Identify the parasite.
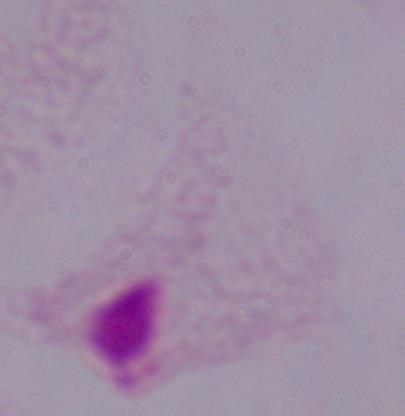

A trichomonad.

Captured at 1000x magnification. Photomicrograph.